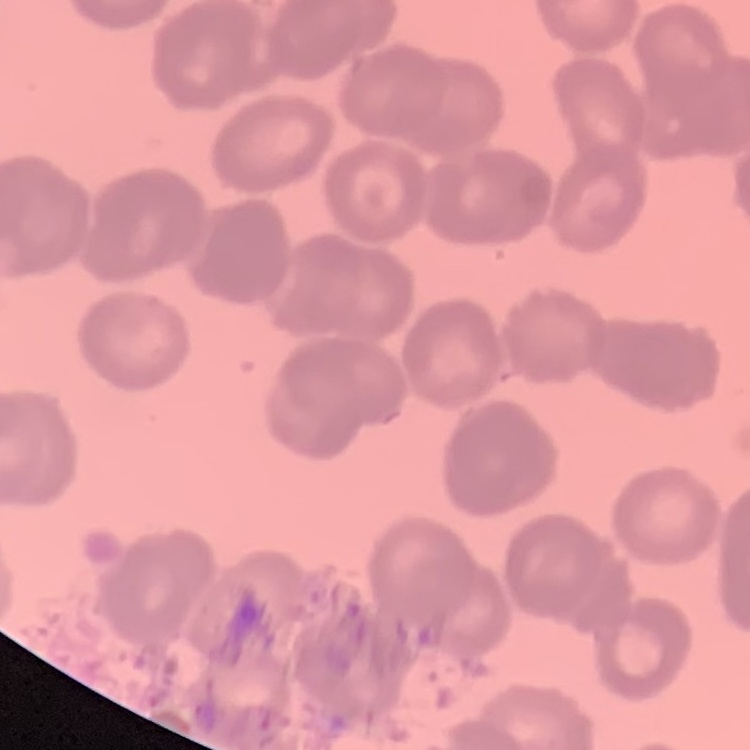

The erythrocytes show rouleaux formation. Square crop of a larger photomicrograph. Field's or Giemsa stain. Thin blood smear.